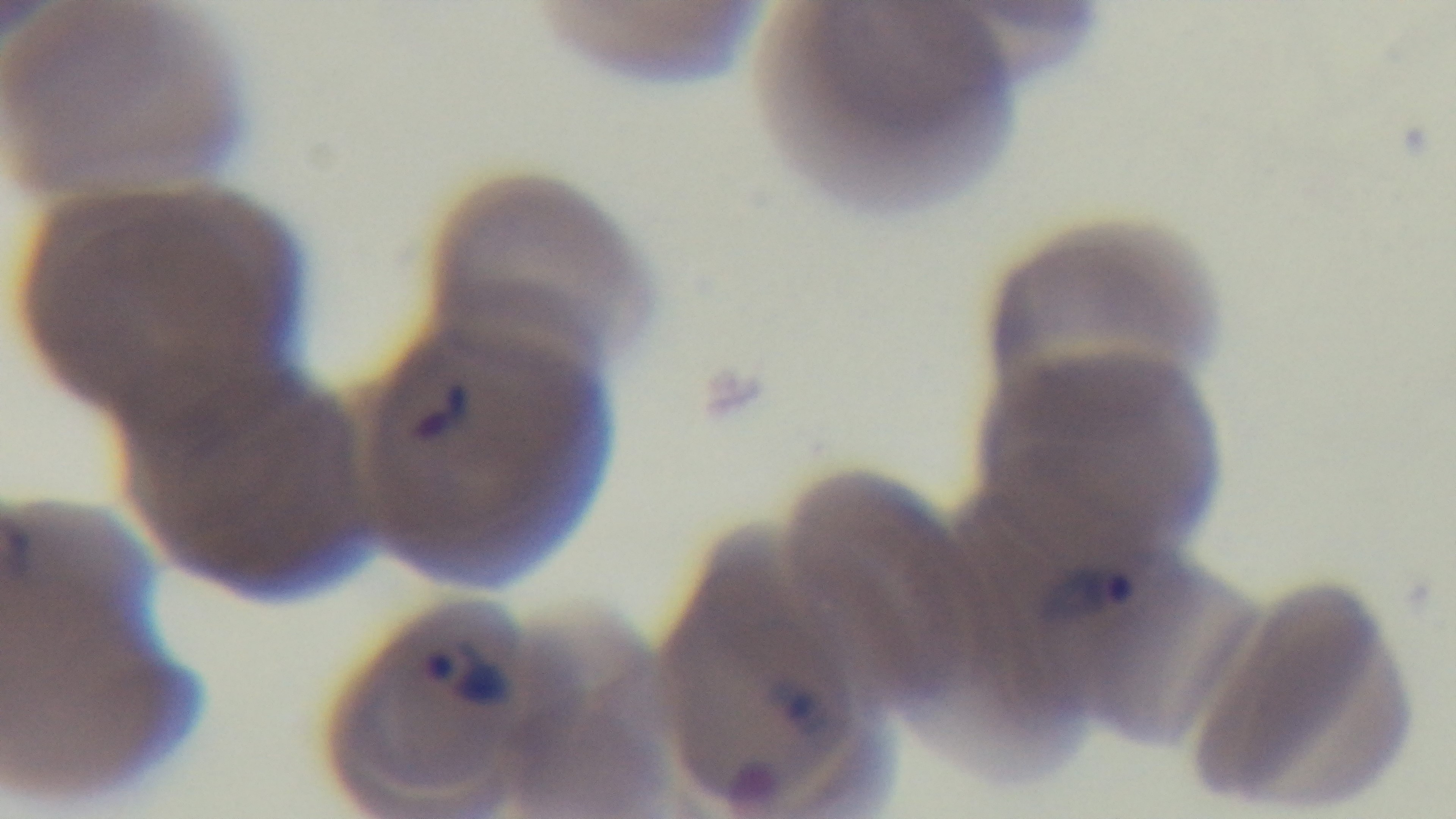
Summary:
  - Malaria status: infected
  - Preparation: thin
  - Objective: 100x oil immersion
  - Capture: mounted 4K digital camera
  - Stain: Giemsa
  - Field of view: one from the slide
  - Modality: light microscopy